State the preparation type.
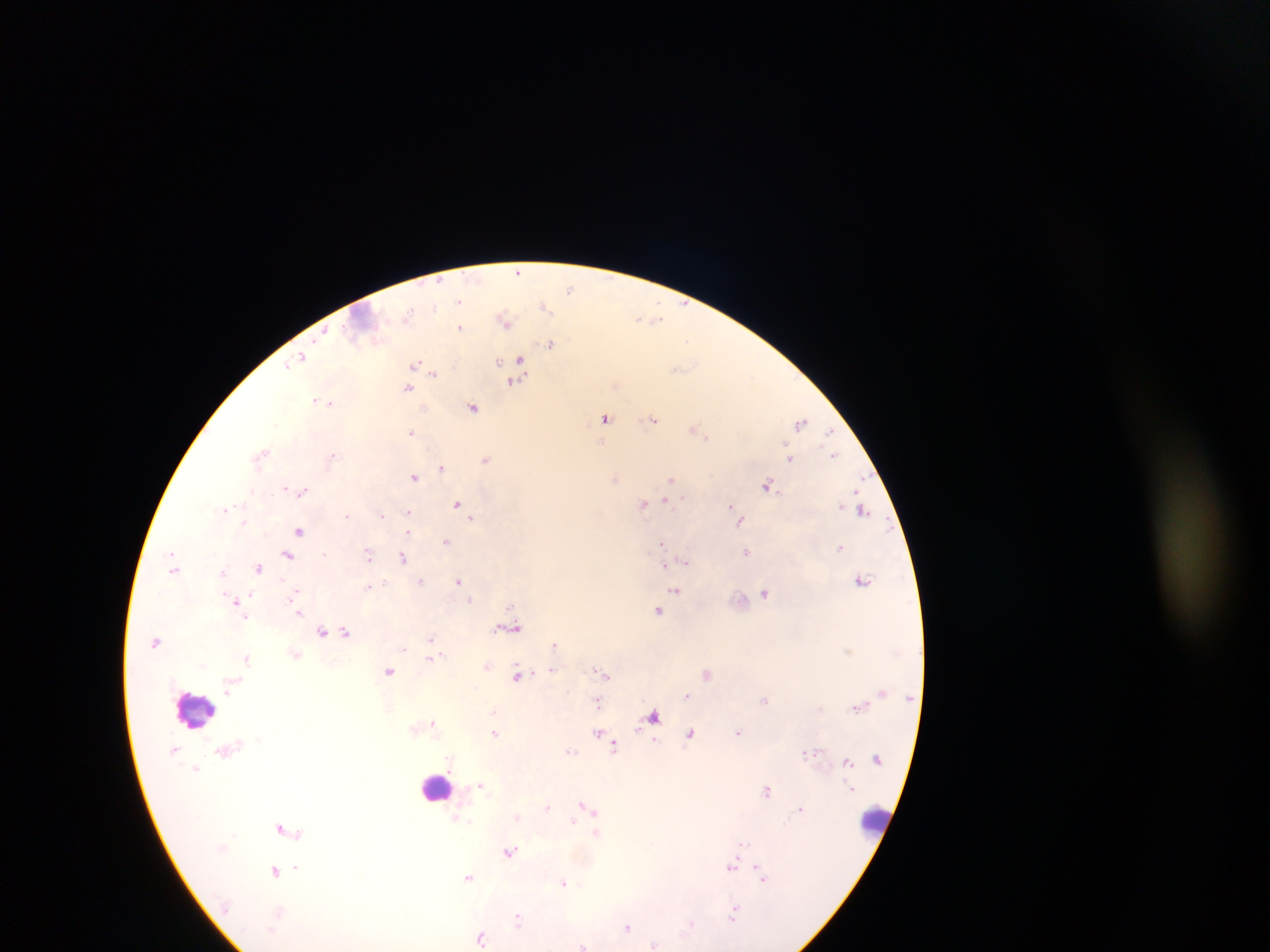

Thick blood smear.

Approximate centers as [x, y] in pixels. Leukocyte locations: [193, 709], [436, 787], [875, 817]. Plasmodium parasite locations: [518, 271], [570, 288], [458, 301], [684, 303], [545, 306], [435, 307], [408, 313], [649, 318], [505, 319], [639, 319], [656, 319], [460, 327], [323, 334], [688, 341], [549, 345], [302, 357], [498, 360], [519, 360], [415, 363], [289, 364], [678, 368], [435, 373], [753, 375], [516, 381], [407, 387], [315, 400], [330, 402], [473, 408], [606, 417], [653, 419], [801, 422], [695, 429], [411, 431], [830, 432], [700, 433], [706, 437], [263, 453], [332, 455], [833, 455], [790, 456], [486, 459], [442, 467], [414, 477], [616, 478], [671, 479], [861, 481], [769, 485], [286, 488], [303, 491], [681, 499], [666, 501], [457, 503], [643, 504], [730, 505], [224, 509], [863, 510], [407, 512], [347, 515], [382, 515], [471, 519], [244, 522], [740, 522], [299, 531], [407, 532], [446, 541], [661, 543], [841, 547], [746, 552], [324, 553], [288, 554], [368, 554], [403, 558], [685, 562], [664, 567], [259, 568], [173, 570], [458, 580], [863, 580], [421, 581], [368, 586], [676, 591], [765, 593], [296, 594], [250, 595], [470, 600], [234, 601], [511, 606], [658, 610], [297, 613], [244, 617], [510, 628], [322, 631], [347, 632], [431, 638], [155, 642], [554, 644], [431, 647], [440, 655], [246, 658], [430, 659], [552, 670], [388, 671], [603, 673], [707, 673], [517, 676], [608, 676], [687, 695], [764, 700], [598, 702], [858, 708], [493, 711], [654, 716], [434, 723], [494, 733], [598, 733], [738, 733], [690, 734], [603, 739], [655, 741], [614, 746], [570, 750], [807, 752], [847, 762], [196, 768], [481, 785], [767, 790], [584, 805], [548, 807], [801, 808], [518, 816], [573, 821], [280, 828], [597, 832], [743, 843], [510, 852], [732, 866], [296, 868], [275, 870], [758, 871], [469, 876], [763, 878], [564, 882], [733, 914], [518, 917], [690, 925], [627, 927], [481, 937], [654, 944], [583, 946]. Image is 1270×952 pixels. Single field of view. Collected in Ghana. Mobile-phone photograph taken through the microscope.